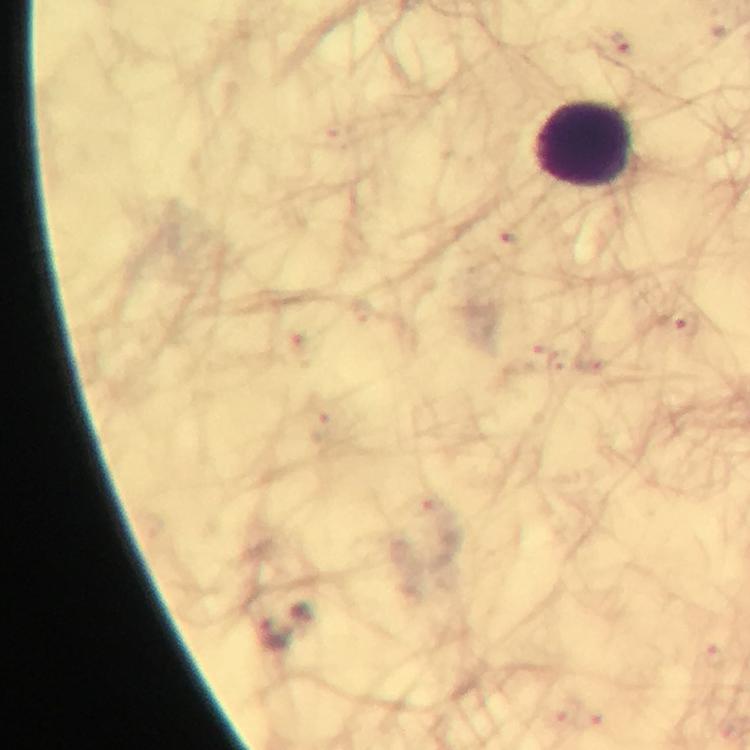

Approximate object centers, in pixels from the top-left corner.
Summary:
  - Malaria parasite locations: (x=619, y=46), (x=680, y=325), (x=275, y=634)
  - Leukocyte locations: (x=585, y=143)
  - Image size: 750×750 pixels
  - Preparation: thick blood film
  - Context: from a malaria diagnostic workup
  - Stain: Giemsa
  - Magnification: 100x
  - Capture: smartphone mounted on the microscope
  - Immersion oil: applied
  - Cropped from: one field of view